State which parasite is depicted.
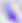
This is Toxoplasma gondii.

Photomicrograph. Captured at 400x magnification.